Locate every blood parasite and identify its species.
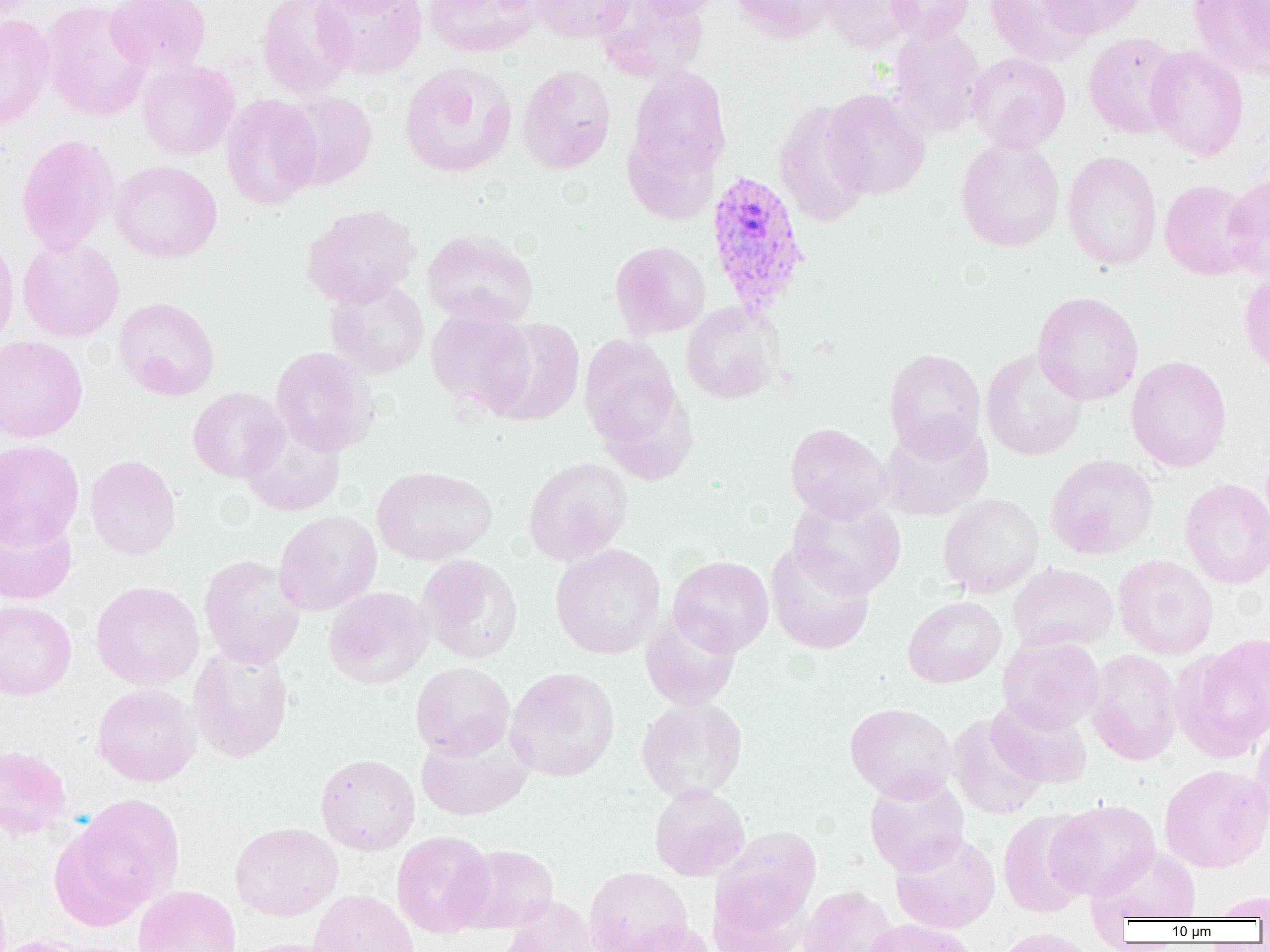
Approximate bounding boxes as named x1/y1/x2/y2 corners in pixels.
Plasmodium vivax-infected red blood cells: (x1=706, y1=168, x2=811, y2=317).
No Plasmodium falciparum, Plasmodium ovale, Plasmodium malariae, Babesia divergens, or Trypanosoma brucei observed.

Uninfected red blood cell locations: (x1=39, y1=0, x2=153, y2=122), (x1=105, y1=0, x2=211, y2=74), (x1=257, y1=0, x2=356, y2=97), (x1=313, y1=0, x2=427, y2=79), (x1=320, y1=0, x2=420, y2=17), (x1=424, y1=0, x2=542, y2=58), (x1=530, y1=0, x2=633, y2=43), (x1=595, y1=0, x2=709, y2=83), (x1=628, y1=0, x2=725, y2=19), (x1=730, y1=0, x2=837, y2=44), (x1=818, y1=0, x2=920, y2=53), (x1=886, y1=0, x2=974, y2=42), (x1=985, y1=0, x2=1094, y2=66), (x1=1037, y1=0, x2=1146, y2=39), (x1=1187, y1=0, x2=1269, y2=79), (x1=1236, y1=0, x2=1270, y2=58), (x1=0, y1=13, x2=56, y2=130), (x1=887, y1=24, x2=987, y2=138), (x1=1083, y1=32, x2=1185, y2=140), (x1=1145, y1=46, x2=1249, y2=161), (x1=966, y1=52, x2=1071, y2=153), (x1=136, y1=60, x2=239, y2=160), (x1=399, y1=62, x2=517, y2=177), (x1=516, y1=65, x2=616, y2=174), (x1=627, y1=66, x2=731, y2=183), (x1=821, y1=89, x2=931, y2=199), (x1=276, y1=90, x2=378, y2=190), (x1=220, y1=94, x2=322, y2=210), (x1=772, y1=99, x2=874, y2=227), (x1=16, y1=133, x2=120, y2=255), (x1=955, y1=138, x2=1064, y2=252), (x1=1062, y1=150, x2=1162, y2=270), (x1=108, y1=159, x2=222, y2=263), (x1=1221, y1=172, x2=1270, y2=281), (x1=1159, y1=179, x2=1259, y2=280), (x1=301, y1=204, x2=421, y2=308), (x1=422, y1=230, x2=538, y2=328), (x1=0, y1=231, x2=20, y2=351), (x1=17, y1=238, x2=124, y2=343), (x1=610, y1=240, x2=711, y2=340), (x1=1239, y1=271, x2=1270, y2=376), (x1=325, y1=278, x2=428, y2=378), (x1=1033, y1=292, x2=1143, y2=405), (x1=113, y1=297, x2=220, y2=401), (x1=681, y1=302, x2=782, y2=404), (x1=426, y1=308, x2=535, y2=414), (x1=482, y1=319, x2=585, y2=426), (x1=0, y1=335, x2=88, y2=443), (x1=579, y1=335, x2=683, y2=452), (x1=271, y1=346, x2=378, y2=456), (x1=884, y1=348, x2=986, y2=459), (x1=980, y1=349, x2=1088, y2=461), (x1=1125, y1=355, x2=1232, y2=473), (x1=188, y1=387, x2=288, y2=483), (x1=240, y1=418, x2=347, y2=517), (x1=878, y1=419, x2=993, y2=521), (x1=785, y1=423, x2=891, y2=522), (x1=0, y1=439, x2=85, y2=548), (x1=84, y1=454, x2=181, y2=560), (x1=1046, y1=455, x2=1158, y2=560), (x1=523, y1=456, x2=633, y2=565), (x1=372, y1=465, x2=498, y2=565), (x1=1180, y1=478, x2=1270, y2=589), (x1=938, y1=494, x2=1044, y2=598), (x1=788, y1=495, x2=906, y2=598), (x1=0, y1=509, x2=77, y2=605), (x1=273, y1=511, x2=382, y2=616), (x1=765, y1=542, x2=874, y2=655), (x1=550, y1=544, x2=665, y2=659), (x1=199, y1=554, x2=305, y2=670), (x1=1113, y1=554, x2=1218, y2=659), (x1=418, y1=555, x2=522, y2=663), (x1=668, y1=556, x2=774, y2=654), (x1=1007, y1=563, x2=1118, y2=653), (x1=90, y1=581, x2=204, y2=690), (x1=324, y1=587, x2=434, y2=689), (x1=902, y1=595, x2=1006, y2=688), (x1=0, y1=601, x2=77, y2=700), (x1=640, y1=608, x2=742, y2=710), (x1=997, y1=635, x2=1105, y2=733), (x1=1174, y1=636, x2=1270, y2=760), (x1=188, y1=646, x2=294, y2=762), (x1=1086, y1=649, x2=1183, y2=765), (x1=410, y1=662, x2=515, y2=759), (x1=506, y1=667, x2=619, y2=782), (x1=91, y1=684, x2=201, y2=786), (x1=636, y1=697, x2=748, y2=803), (x1=987, y1=698, x2=1092, y2=790), (x1=845, y1=703, x2=957, y2=802), (x1=947, y1=713, x2=1046, y2=820), (x1=1251, y1=725, x2=1270, y2=832), (x1=416, y1=726, x2=533, y2=822), (x1=0, y1=744, x2=73, y2=841), (x1=315, y1=753, x2=420, y2=855), (x1=1159, y1=764, x2=1270, y2=873), (x1=864, y1=774, x2=969, y2=876), (x1=649, y1=784, x2=750, y2=881), (x1=61, y1=794, x2=185, y2=920), (x1=1050, y1=799, x2=1160, y2=900), (x1=997, y1=809, x2=1097, y2=918), (x1=230, y1=822, x2=343, y2=921), (x1=713, y1=826, x2=821, y2=931), (x1=391, y1=830, x2=495, y2=938), (x1=890, y1=831, x2=1000, y2=934), (x1=455, y1=843, x2=559, y2=933), (x1=1088, y1=846, x2=1201, y2=925), (x1=584, y1=866, x2=693, y2=952), (x1=707, y1=873, x2=815, y2=951), (x1=133, y1=885, x2=241, y2=952), (x1=799, y1=886, x2=899, y2=952), (x1=309, y1=889, x2=419, y2=952), (x1=1207, y1=890, x2=1270, y2=921), (x1=498, y1=896, x2=603, y2=952), (x1=863, y1=919, x2=980, y2=952), (x1=617, y1=920, x2=718, y2=952), (x1=993, y1=928, x2=1101, y2=952), (x1=0, y1=935, x2=99, y2=952), (x1=236, y1=938, x2=344, y2=952). Slide-level diagnosis: Plasmodium vivax. Image is 1270×952 pixels. Thin blood smear. 1000x magnification. One field of a larger specimen. Optical microscopy.